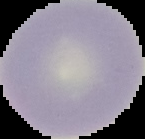

Result: no malaria parasites seen. From a thin blood film. Cell region segmented out of the field of view; the surrounding area is masked to black. Image is 145×139 pixels.